Outline each Plasmodium falciparum-infected red blood cell.
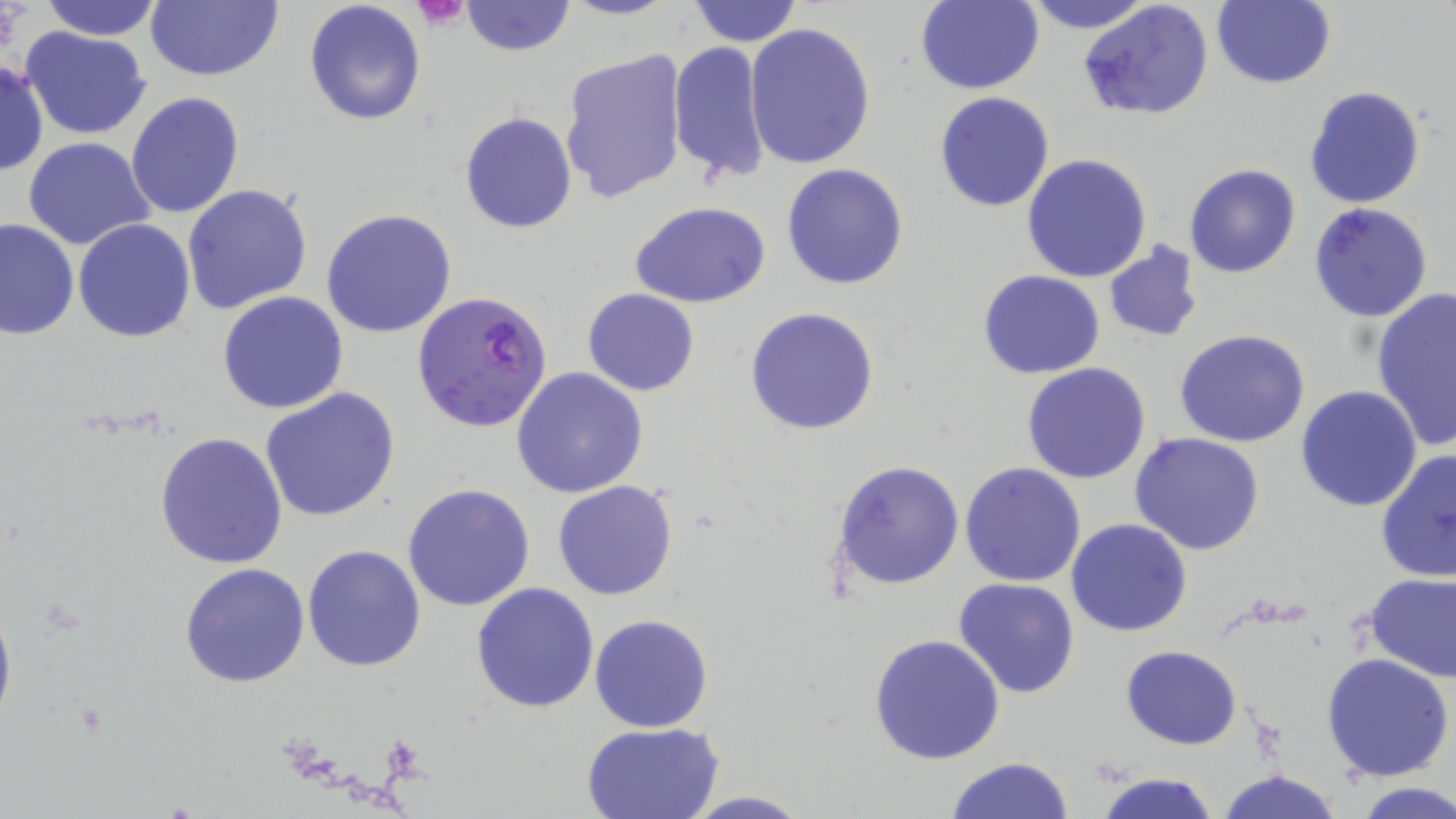
Approximate bounding boxes as (x1,y1)-(x2,y2) corner pairs in pixels.
Plasmodium falciparum-infected red blood cells: (411,289)-(552,434).

slide_level_diagnosis: Plasmodium falciparum
image_size: 1456×819 pixels
uninfected_red_blood_cell_locations: 'approximate bounding boxes as (x1,y1)-(x2,y2) corner pairs in pixels: (34,0)-(168,41), (144,0)-(283,82), (303,0)-(427,127), (461,0)-(574,55), (557,0)-(677,21), (686,0)-(803,47), (914,0)-(1043,95), (1022,0)-(1157,33), (1079,0)-(1214,123), (1211,0)-(1335,88), (745,22)-(876,170), (21,27)-(152,141), (669,40)-(772,183), (560,48)-(691,206), (0,58)-(48,178), (1303,85)-(1427,210), (125,91)-(244,220), (934,91)-(1055,212), (460,111)-(577,232), (24,136)-(156,250), (1021,154)-(1153,284), (782,163)-(910,289), (1184,164)-(1301,278), (182,185)-(313,316), (1308,201)-(1435,323), (631,202)-(770,309), (321,208)-(457,339), (1,218)-(79,340), (74,219)-(196,341), (1102,244)-(1205,343), (977,270)-(1105,379), (1370,287)-(1455,452), (582,288)-(701,396), (217,290)-(349,413), (745,306)-(880,435), (1175,329)-(1310,446), (1022,362)-(1151,483), (512,368)-(648,499), (1295,385)-(1424,513), (260,386)-(403,522), (154,432)-(289,569), (1129,433)-(1266,556), (1376,449)-(1456,583), (832,460)-(963,590), (959,461)-(1088,586), (551,481)-(679,601), (402,483)-(535,612), (1066,518)-(1194,637), (301,544)-(427,671), (179,561)-(310,688), (1363,573)-(1455,682), (952,578)-(1079,698), (471,583)-(600,715), (0,589)-(16,738), (589,614)-(713,733), (869,633)-(1005,765), (1121,644)-(1243,748), (1322,652)-(1453,781), (580,721)-(725,819), (945,757)-(1078,818), (1218,770)-(1346,819), (1093,771)-(1221,819), (1353,782)-(1456,817), (680,791)-(814,818)'
field_of_view: single
preparation: thin blood smear
platelet_locations: 'approximate bounding boxes as (x1,y1)-(x2,y2) corner pairs in pixels: (413,0)-(471,31)'
stain: May-Grünwald-Giemsa
magnification: 1000x
modality: light microscopy